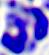
{
  "identification": "white blood cell",
  "modality": "micrograph",
  "magnification": "400x"
}